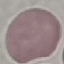
Malaria status: uninfected. Giemsa-stained preparation. Automatically extracted cell patch, resized to 64 × 64 pixels. Thin smear of blood. Acquired by smartphone through the microscope eyepiece.